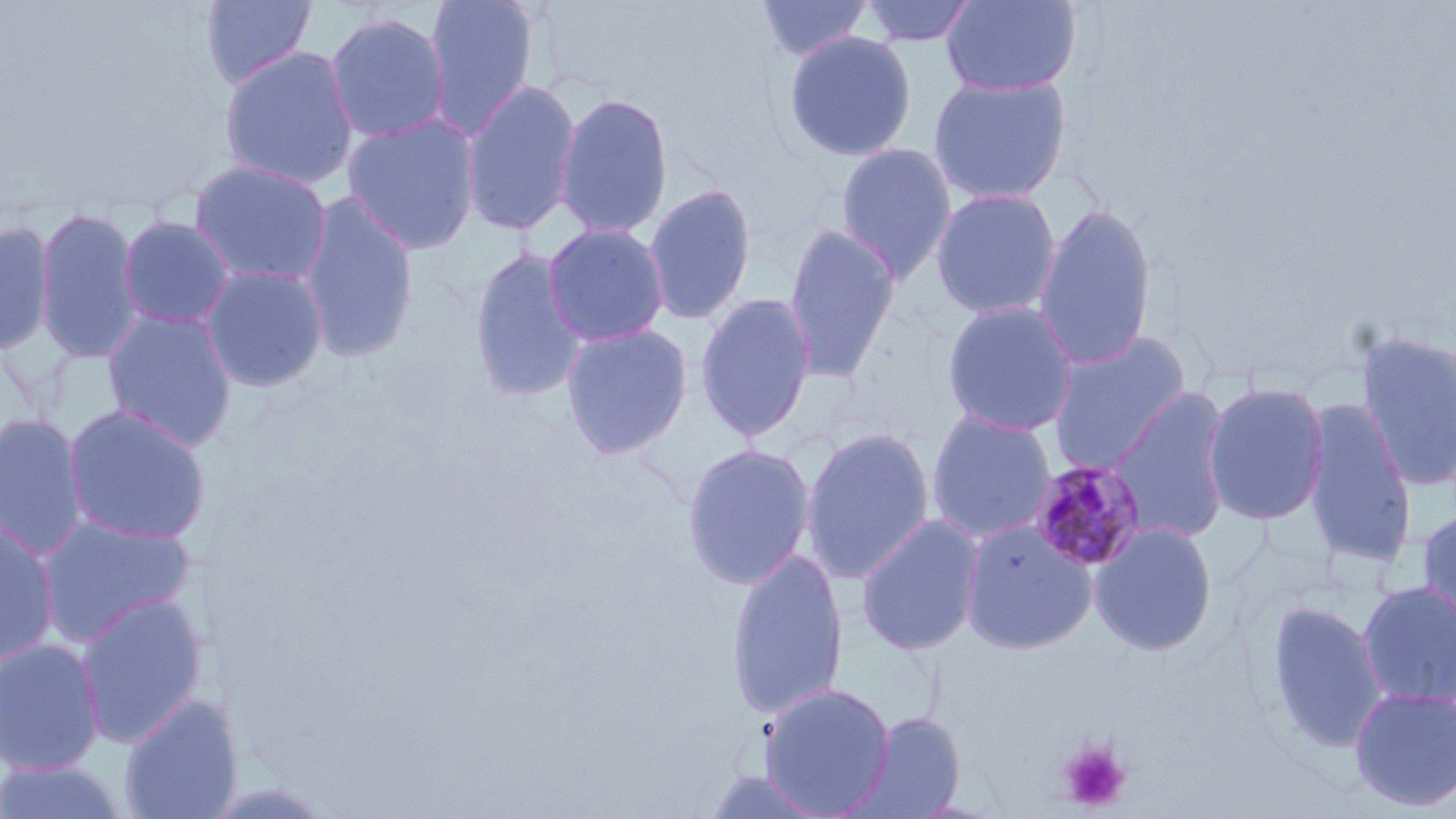
Summary:
  - Coordinate format: approximate bounding boxes as (x1,y1)-(x2,y2) corner pairs in pixels
  - Uninfected red blood cell locations: (199,0)-(318,90), (423,0)-(540,141), (755,0)-(875,62), (941,0)-(1081,97), (856,1)-(980,47), (324,12)-(452,144), (782,32)-(918,162), (218,46)-(359,190), (928,74)-(1071,206), (461,79)-(582,236), (554,92)-(674,239), (342,113)-(481,256), (835,143)-(957,283), (188,159)-(334,288), (643,183)-(758,326), (930,187)-(1062,320), (296,191)-(420,363), (1033,203)-(1158,372), (34,205)-(145,366), (116,215)-(236,329), (0,218)-(56,355), (542,222)-(670,347), (782,223)-(902,383), (467,247)-(589,403), (198,263)-(330,392), (694,292)-(817,442), (941,299)-(1080,437), (102,306)-(239,451), (560,321)-(693,459), (1353,329)-(1456,493), (1046,330)-(1193,474), (1203,381)-(1329,526), (1107,386)-(1233,545), (1300,399)-(1418,571), (62,403)-(212,545), (925,409)-(1057,543), (0,412)-(90,559), (800,426)-(936,583), (680,442)-(816,590), (1416,507)-(1456,644), (36,513)-(196,646), (0,514)-(61,667), (855,515)-(985,657), (960,517)-(1099,655), (1088,521)-(1219,656), (726,548)-(849,720), (1356,580)-(1456,709), (75,592)-(208,748), (1262,599)-(1388,757), (0,638)-(105,775), (759,681)-(896,817), (1348,685)-(1456,812), (119,695)-(242,819), (844,710)-(967,819), (0,760)-(131,818), (701,768)-(833,818)
  - Platelet locations: (1058,740)-(1131,812)
  - Plasmodium malariae-infected red blood cell locations: (1028,458)-(1147,572)
  - Slide-level diagnosis: Plasmodium malariae
  - Field of view: one of a larger specimen
  - Magnification: 1000x
  - Preparation: thin blood smear
  - Image size: 1456×819 pixels
  - Modality: light microscopy
  - Stain: May-Grünwald-Giemsa